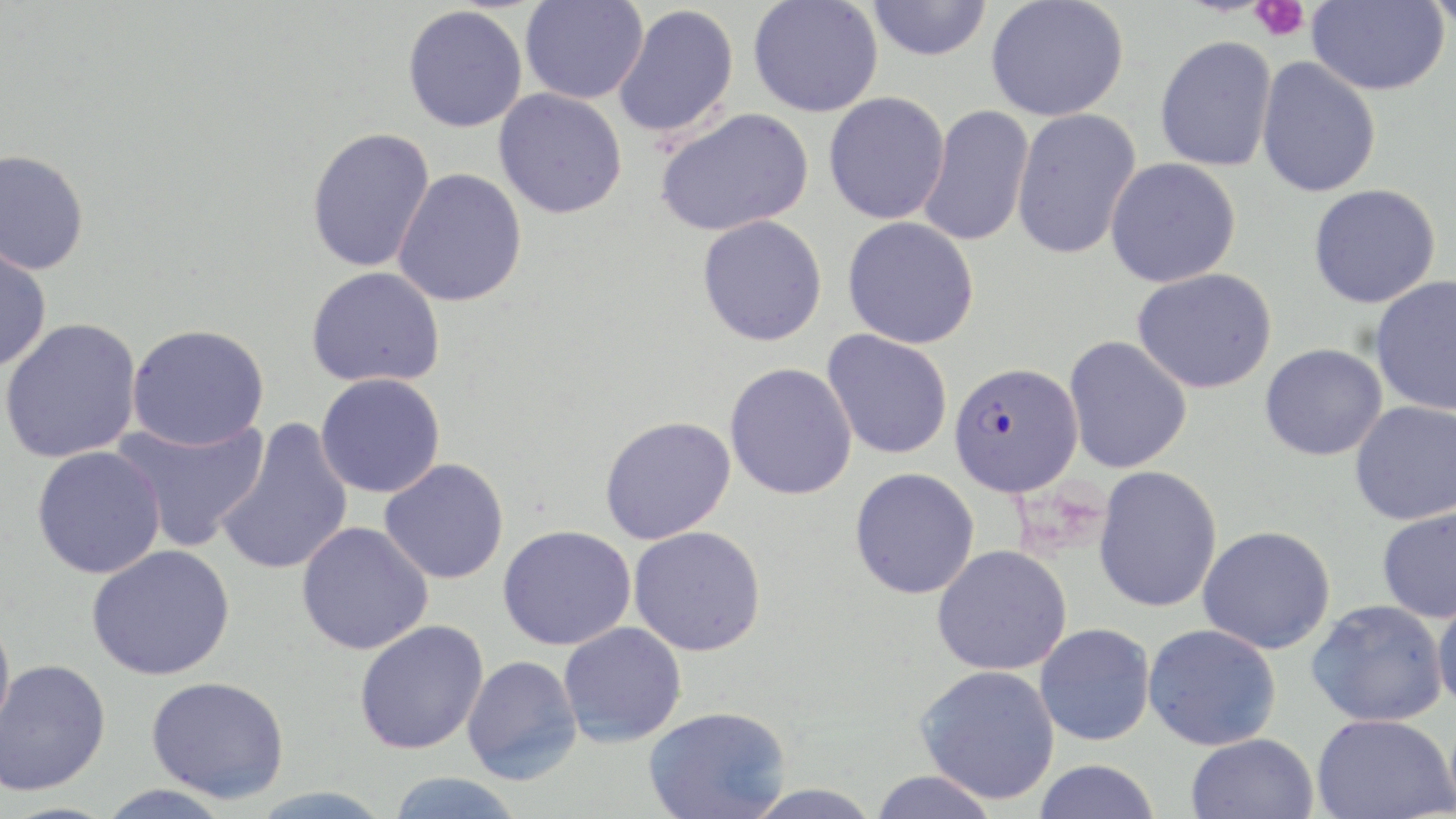
Summary:
  - Coordinate format: approximate bounding boxes as (x1,y1)-(x2,y2) corner pairs in pixels
  - Uninfected red blood cell locations: (748,0)-(883,117), (985,0)-(1129,122), (1306,0)-(1449,95), (1422,0)-(1456,34), (519,1)-(648,104), (865,1)-(994,61), (613,4)-(739,139), (402,5)-(527,132), (1154,35)-(1277,172), (1255,57)-(1381,198), (494,88)-(627,219), (823,91)-(950,225), (917,105)-(1034,247), (655,107)-(814,237), (1011,108)-(1142,260), (305,126)-(436,273), (0,149)-(90,275), (1105,157)-(1241,288), (392,168)-(528,307), (1308,184)-(1442,308), (697,215)-(828,346), (842,217)-(980,349), (0,243)-(52,374), (306,266)-(446,388), (1132,268)-(1278,394), (1370,275)-(1456,416), (0,317)-(143,464), (126,323)-(270,450), (822,329)-(953,460), (1063,336)-(1192,475), (1259,343)-(1387,461), (724,362)-(857,500), (315,373)-(446,498), (1350,400)-(1456,525), (111,415)-(269,553), (599,415)-(736,544), (214,418)-(354,577), (31,445)-(165,579), (379,458)-(509,584), (1093,465)-(1223,613), (849,467)-(980,599), (1376,506)-(1456,623), (296,521)-(433,655), (498,524)-(637,650), (1197,525)-(1336,654), (629,526)-(767,657), (87,544)-(235,681), (932,544)-(1072,676), (1432,590)-(1456,716), (1306,599)-(1448,727), (0,610)-(16,744), (354,619)-(489,755), (558,622)-(687,747), (1035,623)-(1155,746), (1142,624)-(1282,751), (462,654)-(583,785), (0,658)-(111,797), (916,664)-(1061,805), (146,676)-(290,803), (643,706)-(791,819), (1312,713)-(1455,819), (1185,733)-(1319,819), (1032,759)-(1162,819), (868,769)-(1000,819), (385,772)-(527,819), (96,783)-(235,819)
  - Plasmodium falciparum-infected red blood cell locations: (949,361)-(1082,497)
  - Platelet locations: (1250,0)-(1310,42)
  - Slide-level diagnosis: Plasmodium falciparum
  - Modality: light microscopy
  - Field of view: single
  - Stain: May-Grünwald-Giemsa
  - Image size: 1456×819 pixels
  - Preparation: thin blood smear
  - Magnification: 1000x